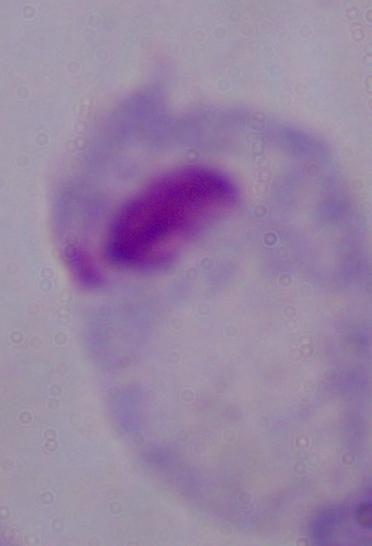
1000x magnification. Micrograph. A trichomonad is shown.